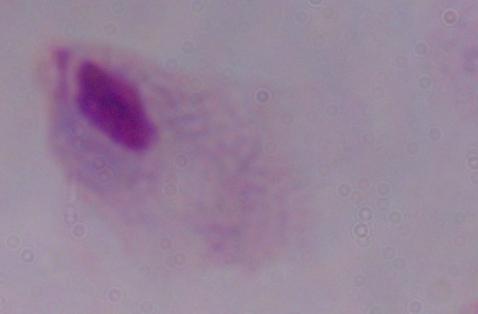
Summary:
  - Magnification: 1000x
  - Identification: trichomonad
  - Modality: micrograph